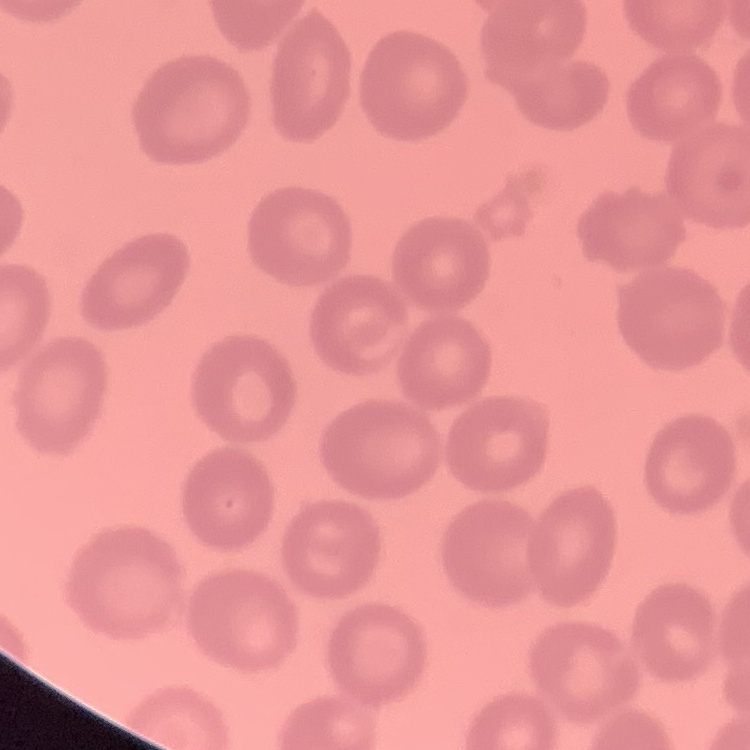
erythrocyte morphology = no rouleaux formation
preparation = thin blood smear
image type = one tile cut from a larger photomicrograph
stain = Field's or Giemsa